Identify the parasite.
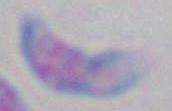

This is Toxoplasma gondii.

Captured at 1000x magnification. Photomicrograph.